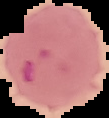

Summary:
  - Image size: 109×118 pixels
  - Image type: cell region segmented out of the field of view; surrounding area masked to black
  - Result: Plasmodium parasites identified
  - Preparation: thin blood film